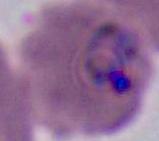

A Plasmodium parasite is seen. Captured at either 400x or 1000x magnification. Micrograph.